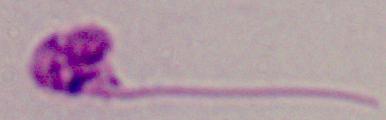
Summary:
  - Modality: photomicrograph
  - Magnification: 1000x
  - Identification: Leishmania